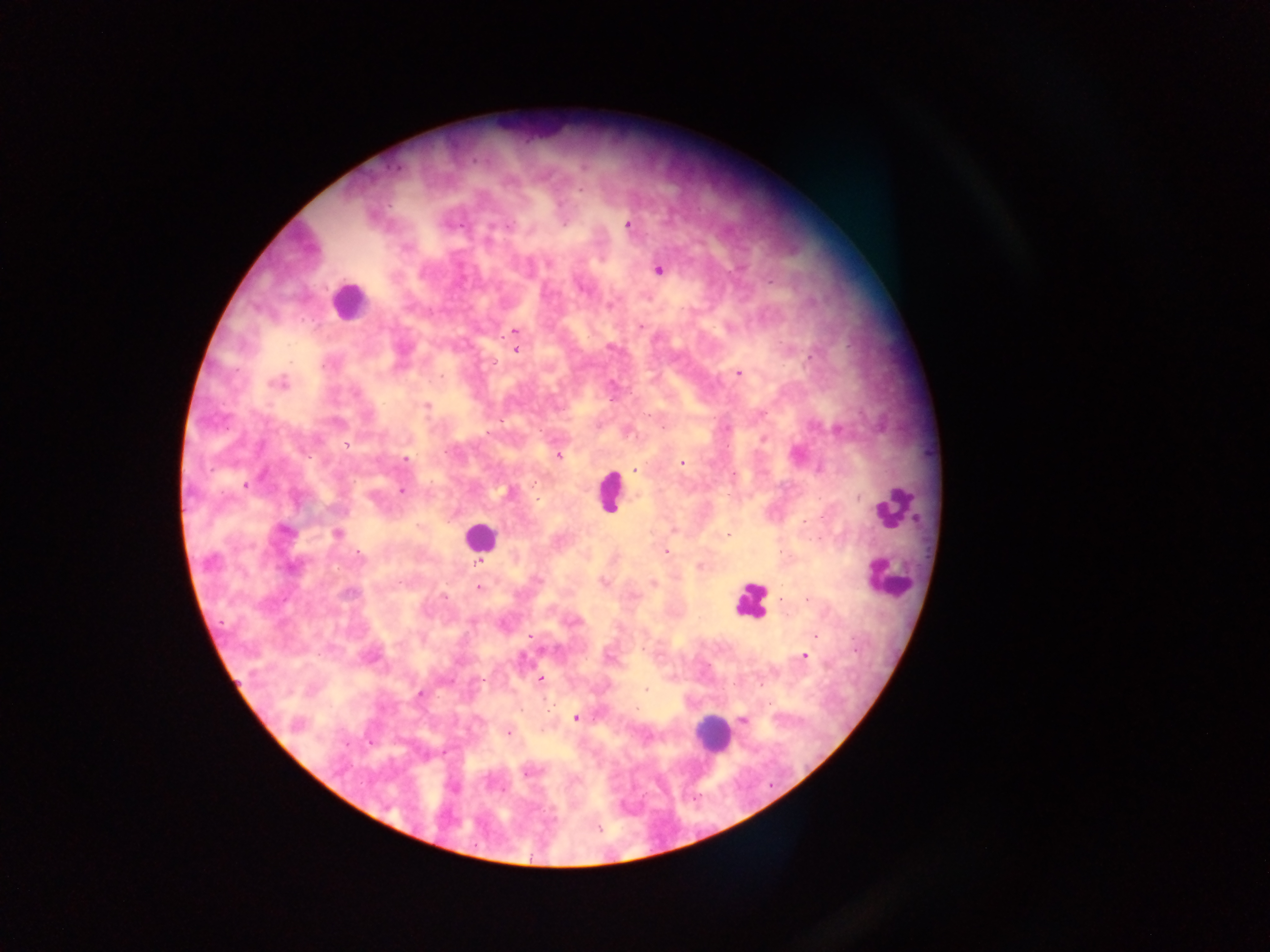
Approximate centers as [x, y] in pixels. Plasmodium parasite locations: [627, 224], [509, 225], [548, 263], [658, 270], [640, 326], [514, 331], [516, 350], [811, 357], [738, 374], [278, 384], [426, 405], [763, 414], [647, 416], [725, 428], [839, 430], [763, 439], [346, 444], [559, 457], [406, 459], [682, 463], [634, 469], [245, 484], [402, 491], [284, 530], [673, 530], [338, 533], [728, 535], [666, 552], [361, 557], [210, 562], [480, 563], [699, 566], [604, 581], [479, 587], [349, 593], [444, 596], [782, 600], [530, 636], [815, 636], [608, 656], [804, 656], [540, 678], [760, 684], [645, 690], [420, 693], [638, 708], [576, 718], [743, 720], [296, 725], [508, 732], [530, 772], [598, 827]. Leukocyte locations: [349, 301], [610, 491], [892, 506], [478, 536], [886, 577], [750, 599], [711, 733]. Sample from Ghana. Single field of view. Photographed through a microscope with a mobile-phone camera. Image is 1270×952 pixels. Thick blood smear.